Describe the morphology of the red blood cells.
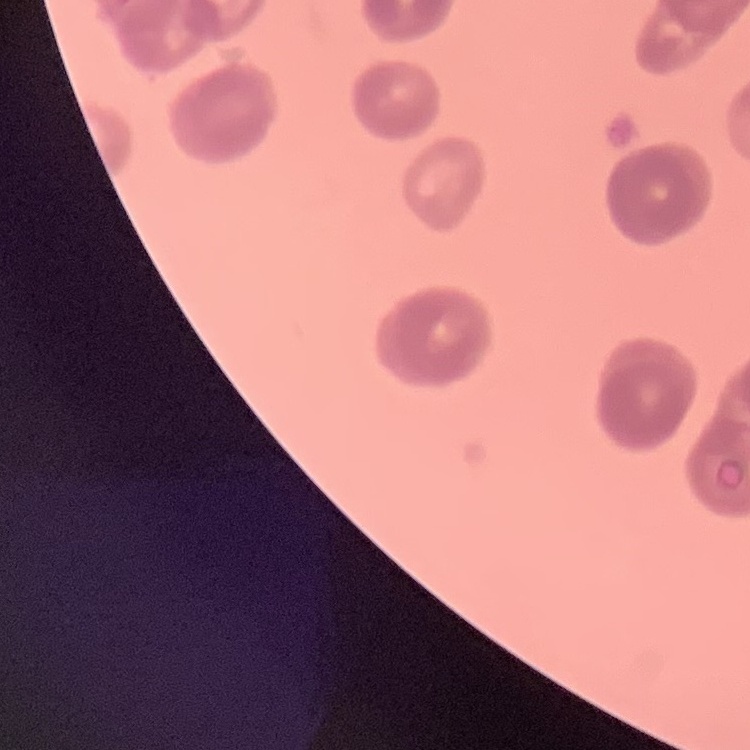
Rouleaux formation.

{
  "preparation": "thin peripheral smear",
  "stain": "Field's or Giemsa",
  "image_type": "square crop of a larger photomicrograph"
}